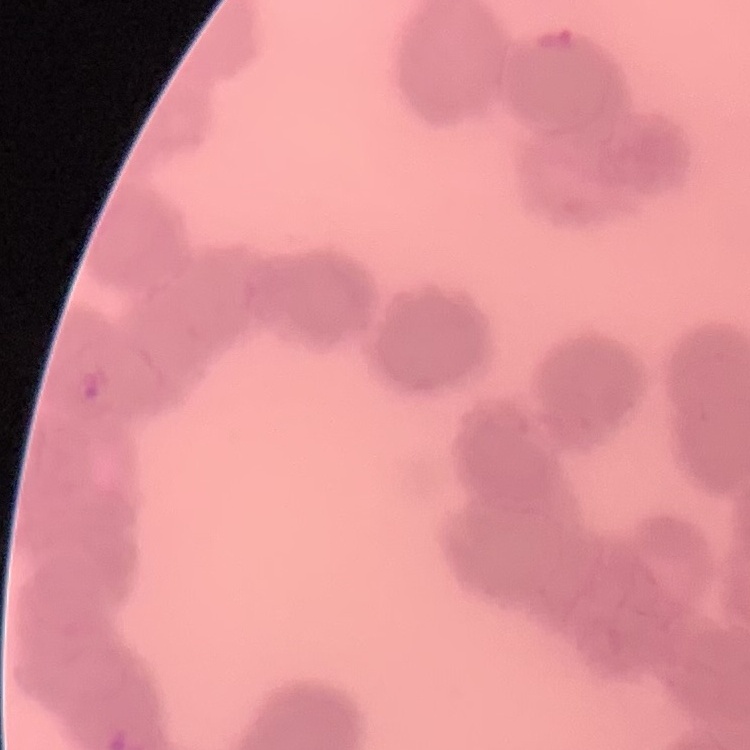
The red blood cells show rouleaux formation. Thin peripheral smear. Square crop of a larger photomicrograph. Field's or Giemsa stain.